Assess the morphology of the erythrocytes.
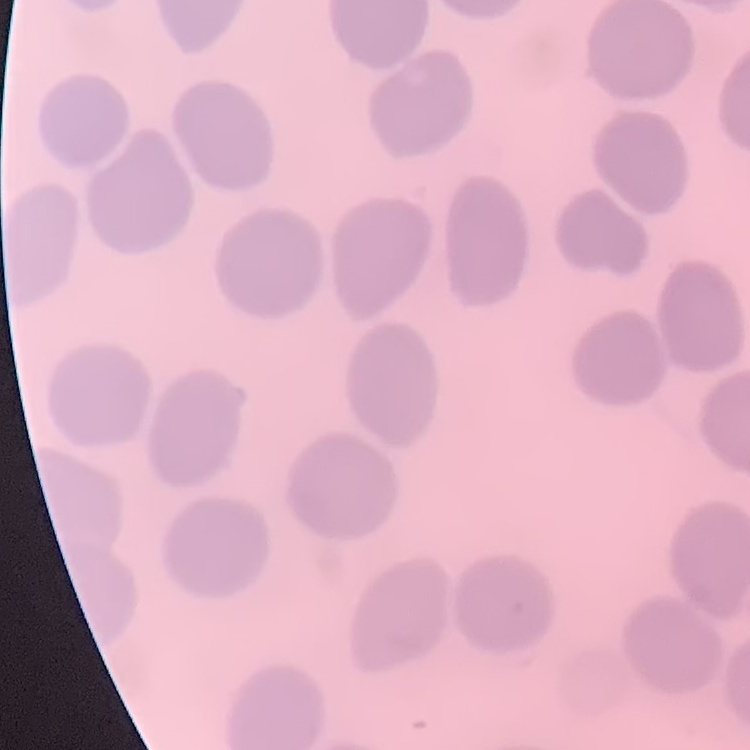

No rouleaux formation.

Summary:
  - Preparation: thin blood film
  - Stain: Field's or Giemsa
  - Image type: one tile cut from a larger photomicrograph